Locate every blood parasite and identify its species.
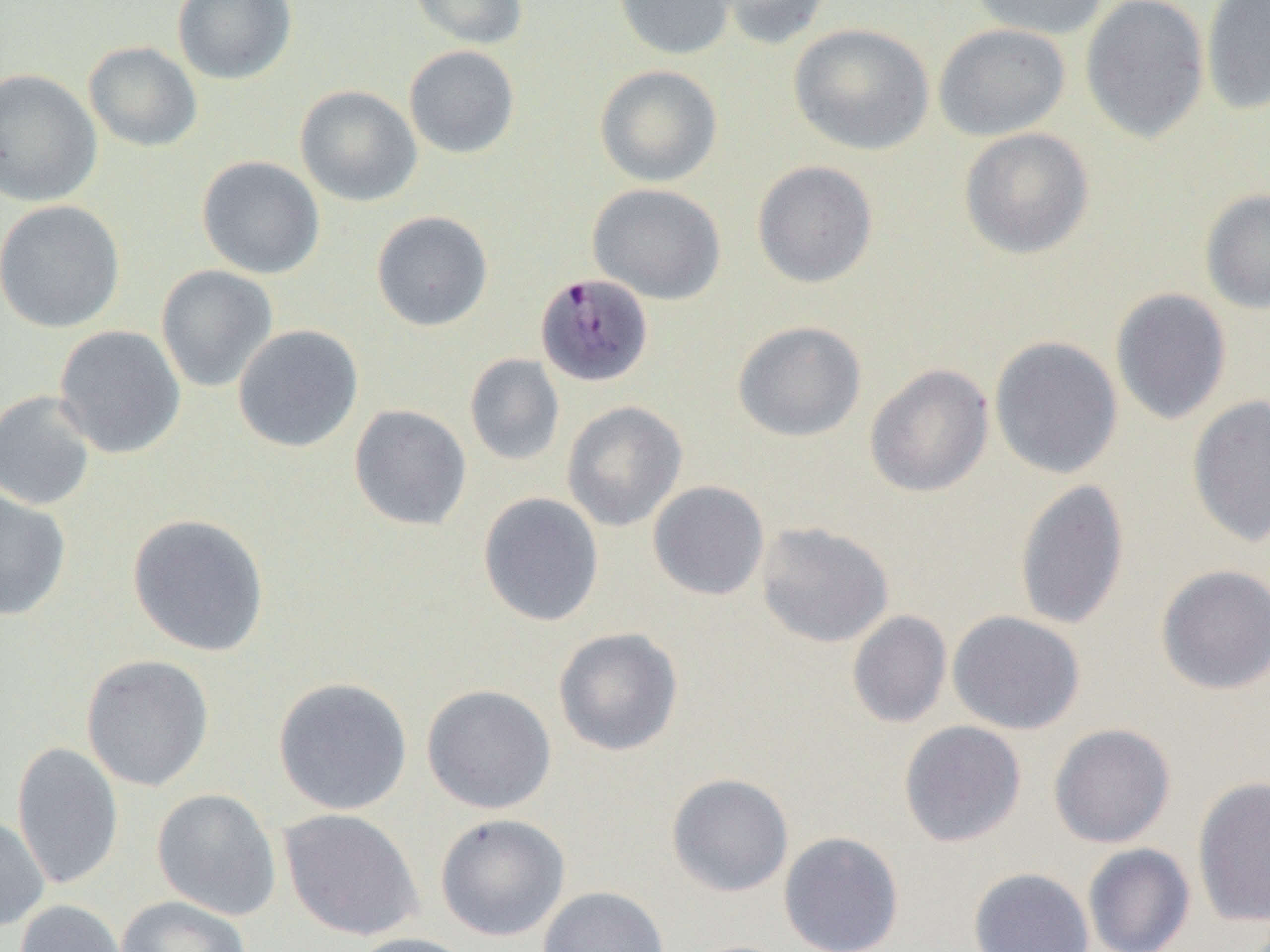

Approximate bounding boxes as (x1, y1, x2, y2) in pixels.
Plasmodium malariae-infected red blood cells: (535, 272, 654, 387).
No Plasmodium falciparum, Plasmodium ovale, Plasmodium vivax, Babesia divergens, or Trypanosoma brucei observed.

slide_level_diagnosis: Plasmodium malariae
preparation: thin blood smear
image_size: 1270×952 pixels
modality: light microscopy
magnification: 1000x
field_of_view: single
uninfected_red_blood_cell_locations: 'approximate bounding boxes as (x1, y1, x2, y2) in pixels: (172, 0, 297, 85), (408, 0, 529, 50), (614, 0, 736, 60), (711, 0, 835, 50), (968, 0, 1111, 40), (1080, 0, 1210, 143), (1201, 0, 1270, 116), (933, 22, 1072, 141), (789, 23, 935, 155), (83, 41, 203, 152), (404, 45, 520, 158), (595, 64, 723, 187), (0, 68, 102, 207), (295, 85, 422, 207), (959, 127, 1094, 259), (196, 155, 325, 279), (752, 160, 878, 288), (587, 182, 726, 305), (1200, 188, 1270, 314), (0, 199, 126, 333), (371, 210, 493, 332), (156, 264, 279, 392), (1110, 288, 1232, 426), (732, 320, 867, 442), (232, 324, 364, 452), (53, 325, 186, 459), (989, 336, 1124, 480), (464, 353, 565, 466), (864, 363, 994, 498), (0, 390, 98, 511), (1187, 395, 1270, 548), (561, 400, 687, 531), (348, 404, 472, 531), (1014, 478, 1130, 632), (647, 481, 770, 601), (0, 489, 72, 621), (478, 492, 604, 627), (127, 513, 270, 657), (755, 521, 894, 648), (1155, 564, 1270, 695), (847, 610, 952, 728), (947, 610, 1085, 734), (553, 627, 684, 756), (81, 654, 215, 792), (273, 676, 413, 815), (421, 684, 557, 815), (899, 720, 1027, 848), (1048, 723, 1176, 848), (12, 741, 123, 890), (666, 773, 794, 897), (1192, 777, 1270, 927), (152, 788, 282, 920), (278, 808, 424, 942), (435, 813, 571, 941), (0, 814, 50, 933), (778, 831, 905, 952), (1083, 843, 1195, 952), (969, 867, 1095, 952), (537, 885, 671, 952), (116, 895, 252, 952), (14, 899, 128, 952), (346, 932, 481, 952)'